Give the preparation type.
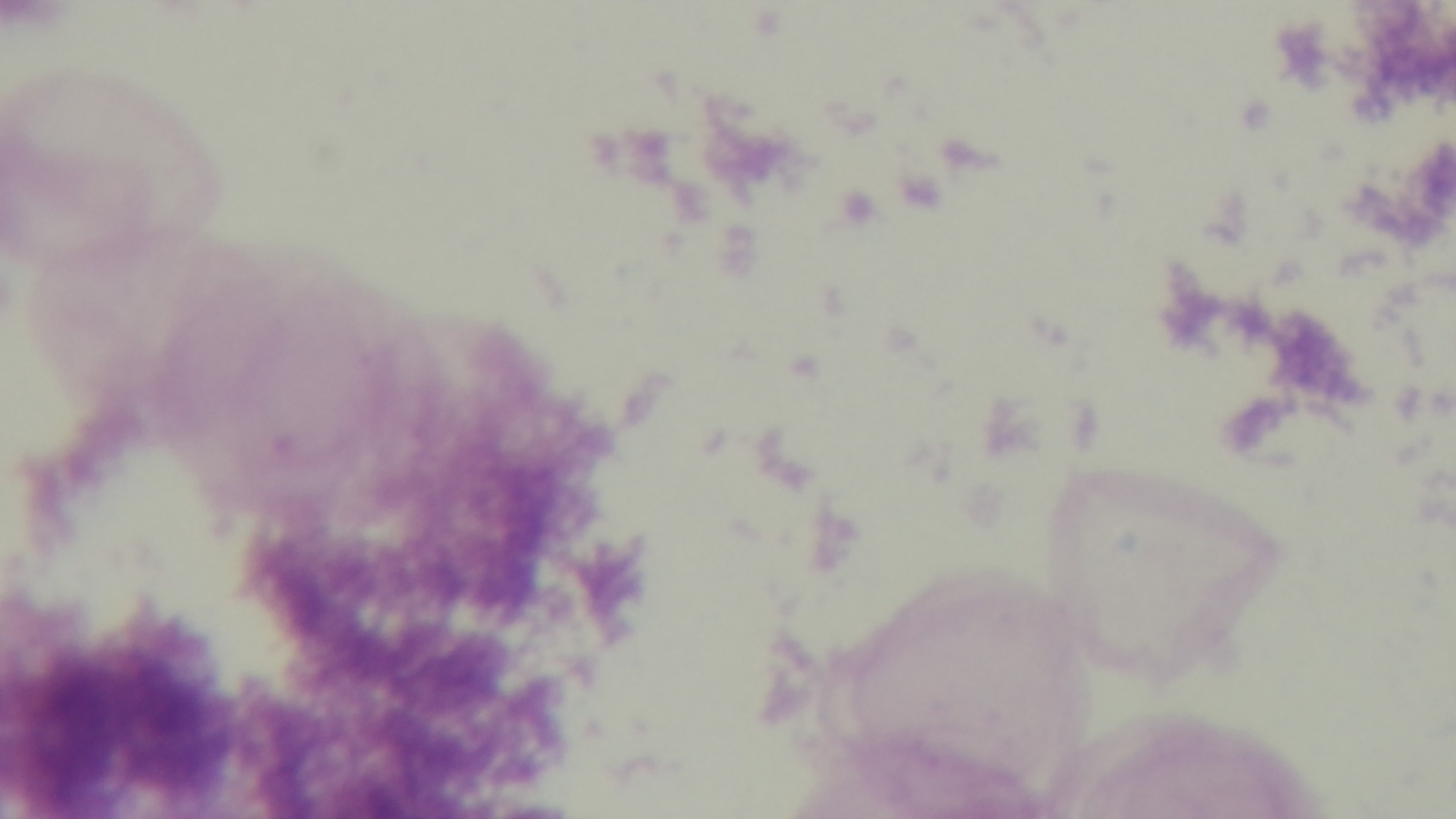
It is a thick blood film.

objective = 100x oil immersion
stain = Giemsa
malaria status = uninfected
field of view = single
modality = light microscopy
capture = mounted 4K digital camera